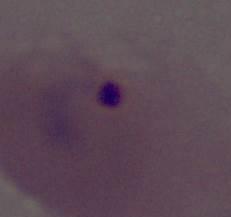

{
  "modality": "micrograph",
  "magnification": "400x or 1000x",
  "identification": "Plasmodium"
}